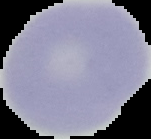
Summary:
  - Image type: cell region segmented out of the field of view; surrounding area masked to black
  - Preparation: thin blood smear
  - Result: no Plasmodium parasites seen
  - Image size: 151×139 pixels